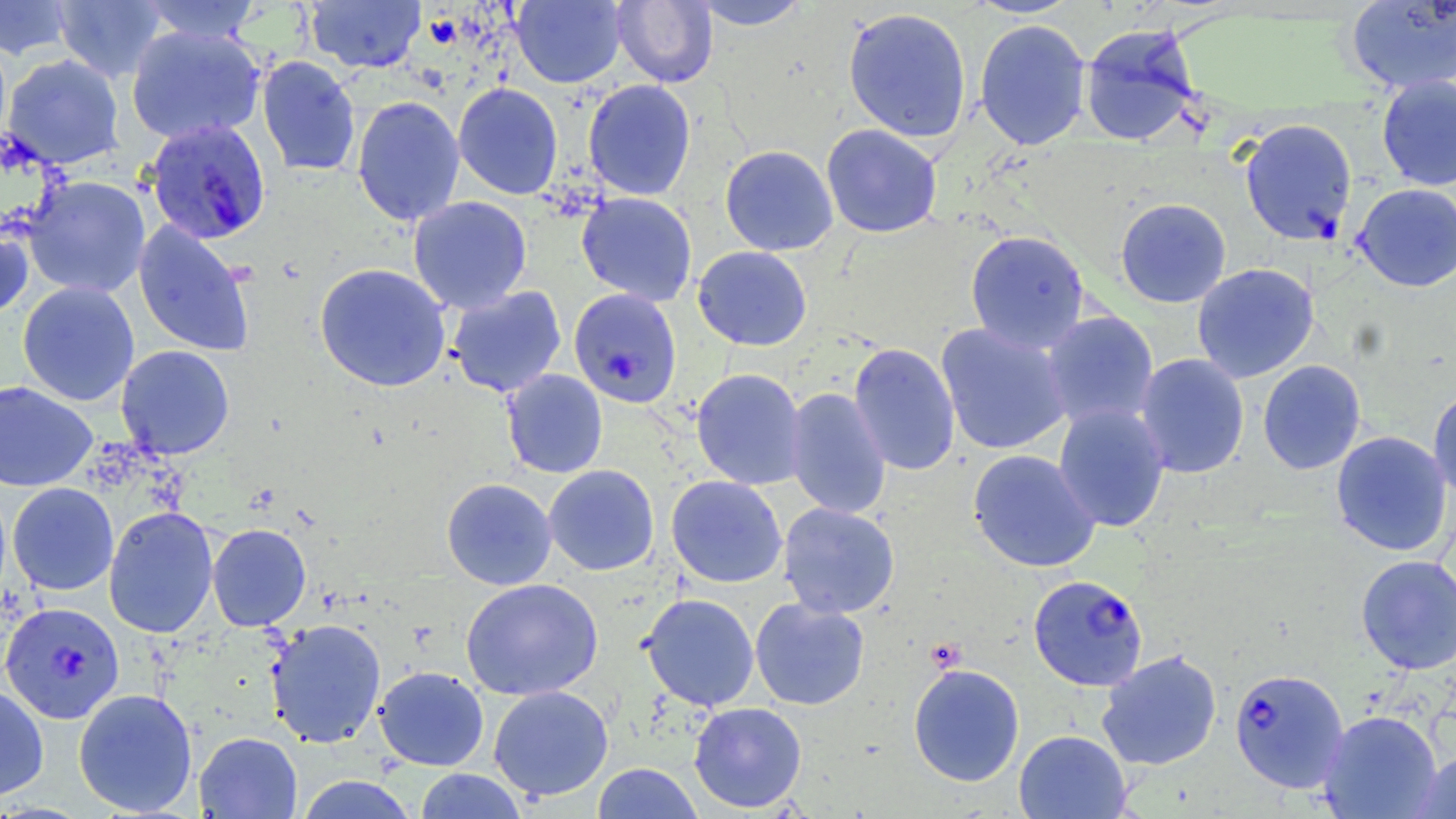
slide-level diagnosis = Plasmodium falciparum
image size = 1456×819 pixels
magnification = 1000x
field of view = one of a larger specimen
Plasmodium falciparum-infected red blood cell locations = approximate bounding boxes as [x1, y1, x2, y2] in pixels: [143, 118, 271, 245], [1238, 118, 1358, 246], [568, 288, 683, 409], [1027, 573, 1149, 692], [0, 601, 124, 723], [1229, 666, 1349, 793]
stain = May-Grünwald-Giemsa
modality = light microscopy
uninfected red blood cell locations = approximate bounding boxes as [x1, y1, x2, y2] in pixels: [0, 0, 76, 60], [53, 0, 167, 82], [139, 0, 262, 44], [305, 0, 426, 73], [511, 0, 627, 88], [690, 0, 811, 30], [612, 1, 718, 88], [1345, 1, 1456, 95], [842, 7, 973, 143], [973, 19, 1092, 150], [1079, 23, 1202, 145], [125, 25, 266, 144], [3, 54, 125, 169], [257, 56, 361, 177], [1375, 74, 1456, 191], [582, 79, 697, 201], [453, 82, 563, 200], [351, 95, 465, 227], [821, 123, 943, 238], [720, 145, 838, 256], [21, 175, 151, 298], [1353, 183, 1456, 291], [576, 192, 698, 306], [408, 196, 532, 314], [1115, 198, 1231, 308], [0, 216, 34, 322], [133, 221, 256, 357], [965, 230, 1090, 353], [692, 245, 813, 351], [314, 263, 452, 392], [1191, 263, 1319, 383], [17, 281, 140, 406], [447, 285, 567, 398], [1040, 310, 1160, 431], [935, 323, 1072, 456], [847, 342, 961, 476], [116, 344, 234, 459], [1134, 353, 1250, 479], [1257, 359, 1366, 475], [691, 368, 807, 490], [501, 369, 608, 478], [0, 381, 98, 492], [784, 387, 891, 519], [1427, 387, 1456, 501], [1053, 403, 1170, 532], [1330, 430, 1453, 557], [967, 449, 1101, 572], [543, 464, 660, 576], [666, 475, 788, 588], [441, 478, 557, 590], [7, 482, 119, 595], [777, 502, 900, 619], [103, 506, 218, 638], [207, 523, 311, 631], [1355, 554, 1456, 674], [460, 578, 603, 700], [639, 593, 759, 711], [750, 597, 870, 710], [265, 618, 387, 748], [1096, 649, 1222, 771], [908, 663, 1025, 787], [374, 666, 489, 771], [0, 683, 49, 802], [488, 685, 614, 801], [73, 688, 198, 816], [688, 701, 807, 813], [1318, 710, 1442, 818], [1014, 729, 1132, 818], [194, 731, 303, 819], [1414, 751, 1456, 818], [592, 762, 704, 819], [414, 768, 527, 818], [295, 774, 419, 819]
preparation = thin blood film